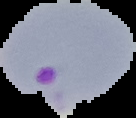

Summary:
  - Malaria status: parasitized
  - Image type: segmented cell region on a black background
  - Preparation: thin blood film
  - Image size: 136×118 pixels